Assess this cell for malaria.
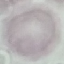

It is uninfected.

capture: smartphone camera at the microscope eyepiece
preparation: thin blood smear
stain: Giemsa
image_type: automatically extracted cell patch, resized to 64 × 64 pixels